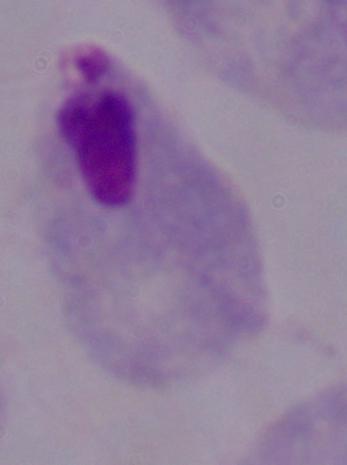

Summary:
  - Modality: photomicrograph
  - Identification: trichomonad
  - Magnification: 1000x